Report the malaria status of this cell.
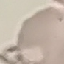

Uninfected.

Summary:
  - Preparation: thin blood film
  - Capture: smartphone camera at the microscope eyepiece
  - Image type: automatically extracted cell patch, resized to 64 × 64 pixels
  - Stain: Giemsa